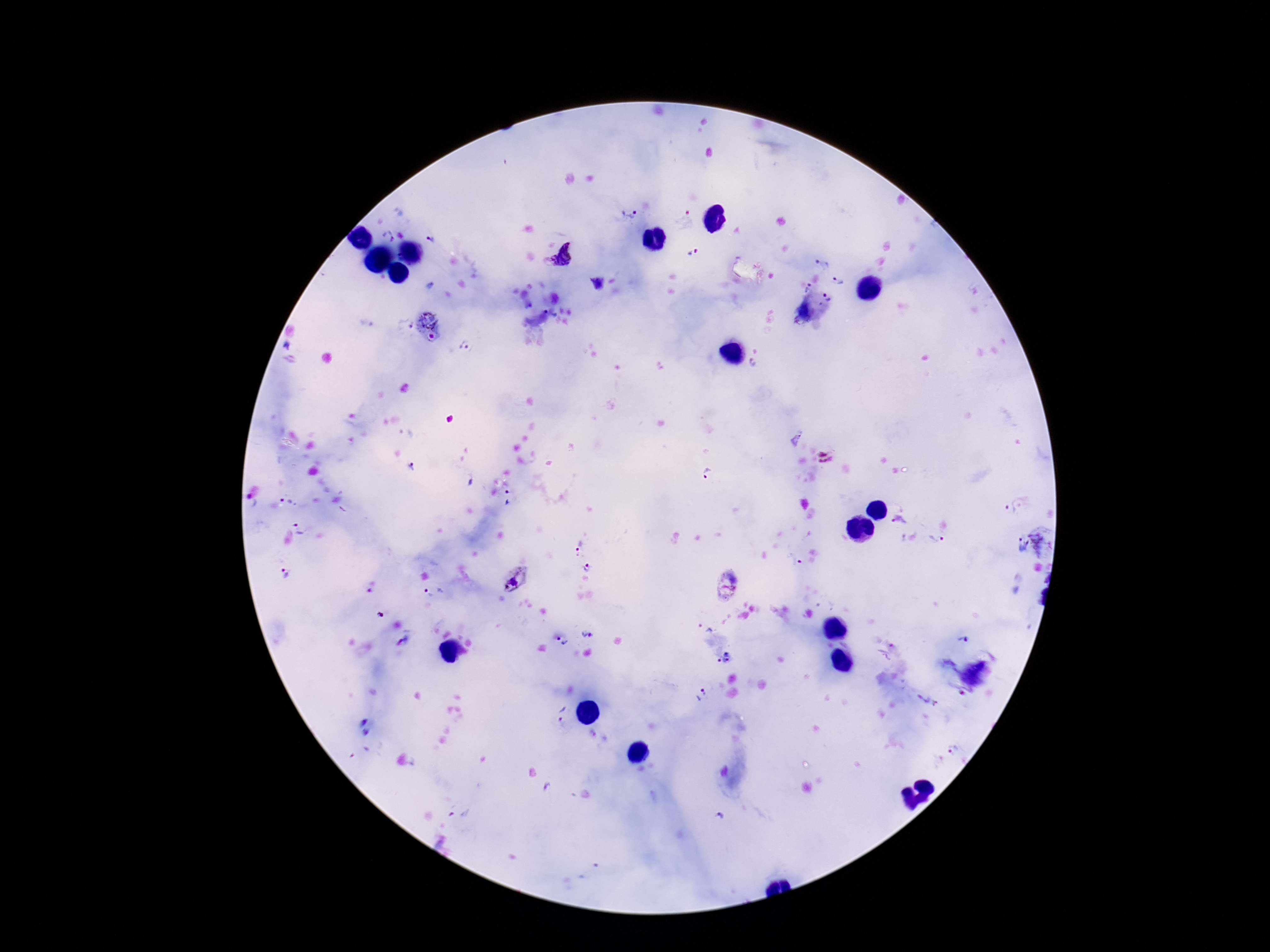
Approximate centers as [x, y] in pixels. Plasmodium parasite locations: [629, 215], [685, 219], [388, 237], [430, 238], [694, 251], [570, 254], [551, 263], [822, 263], [838, 281], [596, 284], [430, 285], [805, 289], [827, 299], [551, 311], [801, 312], [428, 318], [405, 324], [432, 336], [285, 348], [466, 348], [754, 365], [796, 437], [412, 467], [707, 475], [470, 482], [509, 498], [250, 502], [287, 502], [1010, 509], [900, 522], [301, 528], [936, 540], [1021, 544], [1036, 545], [580, 548], [792, 561], [588, 567], [285, 572], [516, 579], [371, 586], [724, 589], [432, 591], [380, 615], [587, 635], [963, 641], [403, 642], [563, 643], [724, 658], [981, 671], [955, 678], [701, 694], [924, 701], [563, 715], [362, 722], [367, 732], [954, 749], [548, 788], [460, 817], [720, 817]. Thick peripheral-blood smear. Patient malaria status: positive. Image is 1270×952 pixels. One field from this slide. Smartphone photograph taken through the microscope eyepiece. Giemsa-stained preparation. 100x magnification.